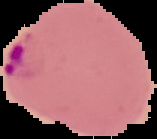
Summary:
  - Preparation: thin blood smear
  - Image size: 157×139 pixels
  - Image type: segmented cell region with the area outside set to black
  - Result: malaria parasites detected